Name the cell type shown.
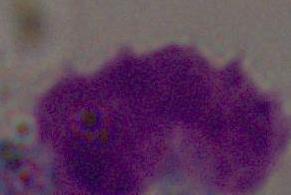
A leukocyte.

Summary:
  - Modality: micrograph
  - Magnification: 1000x